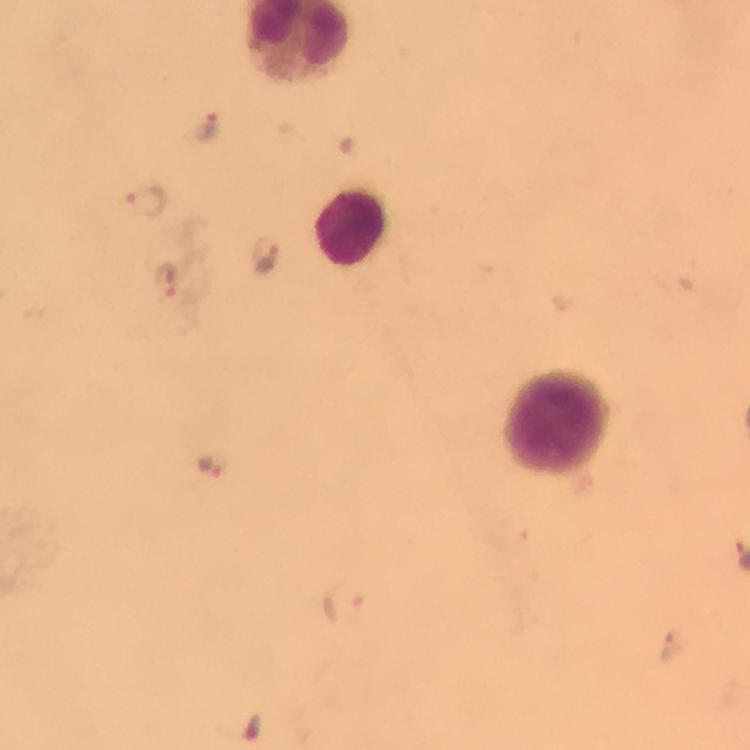

Approximate centers as {x, y} in pixels. Plasmodium parasite locations: {204, 128}, {144, 197}, {266, 256}, {166, 277}, {211, 466}, {343, 603}, {667, 646}. Leukocyte locations: {359, 228}, {558, 420}. A crop from one field of view. Giemsa stain. Image is 750×750 pixels. From a diagnostic examination for malaria. Thick smear. At 100x magnification. Immersion oil was used. Photographed through the microscope with a smartphone camera.